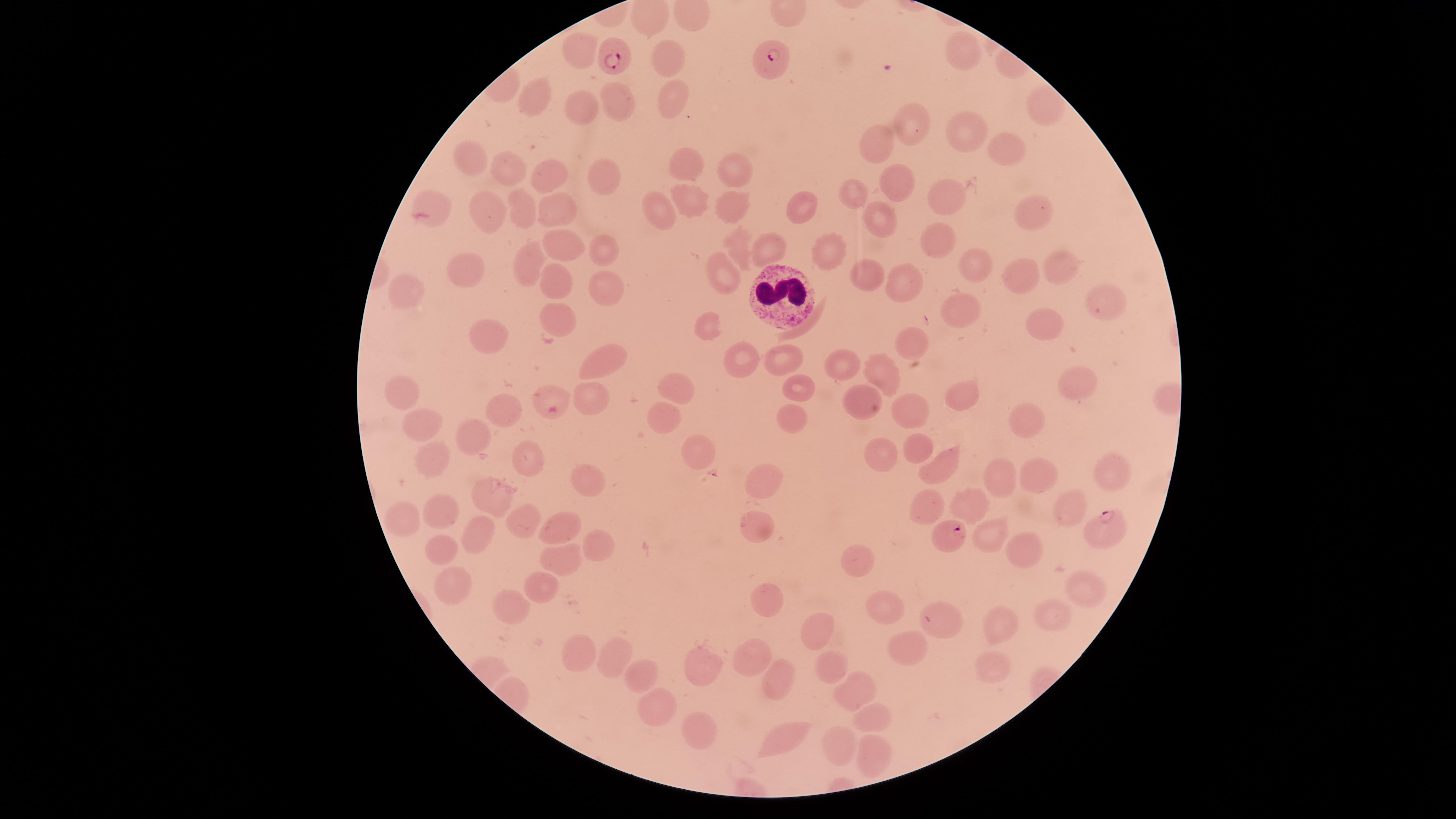

field of view = single
white blood cells = approximate marker points as {x, y} in pixels: {785, 295}
preparation = thin blood film
image size = 1456×819 pixels
visible region = circular
parasitized red blood cells = approximate marker points as {x, y} in pixels: {613, 56}, {768, 59}, {1101, 526}, {946, 536}
presence = malaria parasites detected
uninfected red blood cells = approximate marker points as {x, y} in pixels: {962, 52}, {582, 55}, {671, 57}, {541, 94}, {669, 96}, {621, 104}, {589, 107}, {1041, 110}, {915, 124}, {968, 131}, {1003, 147}, {878, 148}, {468, 159}, {679, 161}, {735, 166}, {516, 169}, {602, 172}, {549, 178}, {893, 180}, {687, 192}, {854, 193}, {949, 195}, {730, 204}, {664, 205}, {800, 205}, {487, 211}, {524, 211}, {561, 211}, {1033, 211}, {437, 216}, {877, 217}, {943, 241}, {744, 247}, {568, 248}, {601, 248}, {772, 252}, {829, 258}, {529, 264}, {970, 264}, {1058, 264}, {473, 270}, {726, 272}, {1011, 272}, {870, 275}, {899, 275}, {555, 277}, {609, 287}, {404, 291}, {1103, 306}, {958, 311}, {554, 314}, {708, 321}, {1041, 324}, {491, 329}, {912, 341}, {743, 354}, {592, 356}, {788, 357}, {841, 368}, {875, 369}, {1076, 382}, {800, 384}, {676, 386}, {968, 390}, {403, 393}, {542, 393}, {587, 394}, {857, 400}, {917, 410}, {505, 411}, {1022, 415}, {667, 417}, {415, 418}, {787, 425}, {473, 437}, {919, 441}, {698, 454}, {881, 456}, {433, 460}, {524, 463}, {940, 468}, {999, 473}, {1106, 473}, {1033, 474}, {581, 478}, {765, 485}, {489, 496}, {926, 502}, {441, 505}, {977, 505}, {1072, 505}, {405, 518}, {526, 522}, {563, 523}, {762, 523}, {988, 531}, {486, 535}, {590, 540}, {437, 545}, {1022, 546}, {567, 558}, {860, 560}, {457, 584}, {540, 586}, {1081, 587}, {765, 601}, {513, 604}, {883, 606}, {1048, 615}, {942, 619}, {997, 627}, {822, 631}, {901, 644}, {578, 653}, {751, 655}, {608, 659}, {693, 662}, {995, 665}, {837, 669}, {635, 672}, {777, 678}, {851, 686}, {657, 706}, {876, 718}, {781, 733}, {697, 734}, {837, 742}, {873, 754}
stain = Giemsa
species = Plasmodium falciparum
capture = smartphone photograph through the microscope eyepiece